Name the parasite shown.
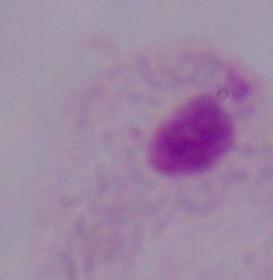
This is a trichomonad.

Summary:
  - Magnification: 1000x
  - Modality: micrograph